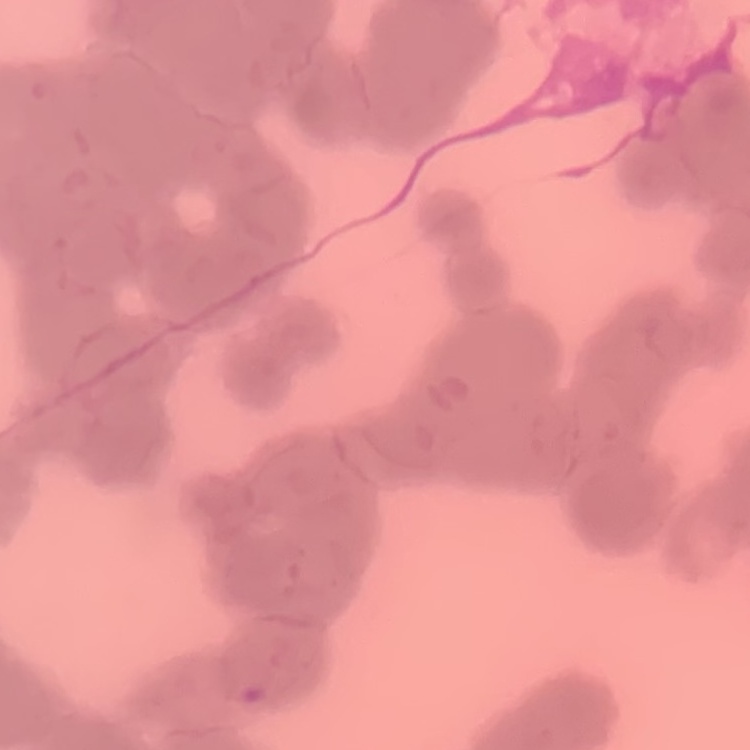

The red blood cells exhibit rouleaux formation. Field's or Giemsa stain. Thin blood film. Square crop of a larger photomicrograph.